Assess this cell for malaria.
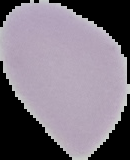

Uninfected.

preparation = thin blood film
image size = 130×160 pixels
image type = cell region segmented out of the field of view; surrounding area masked to black